Classify the preparation.
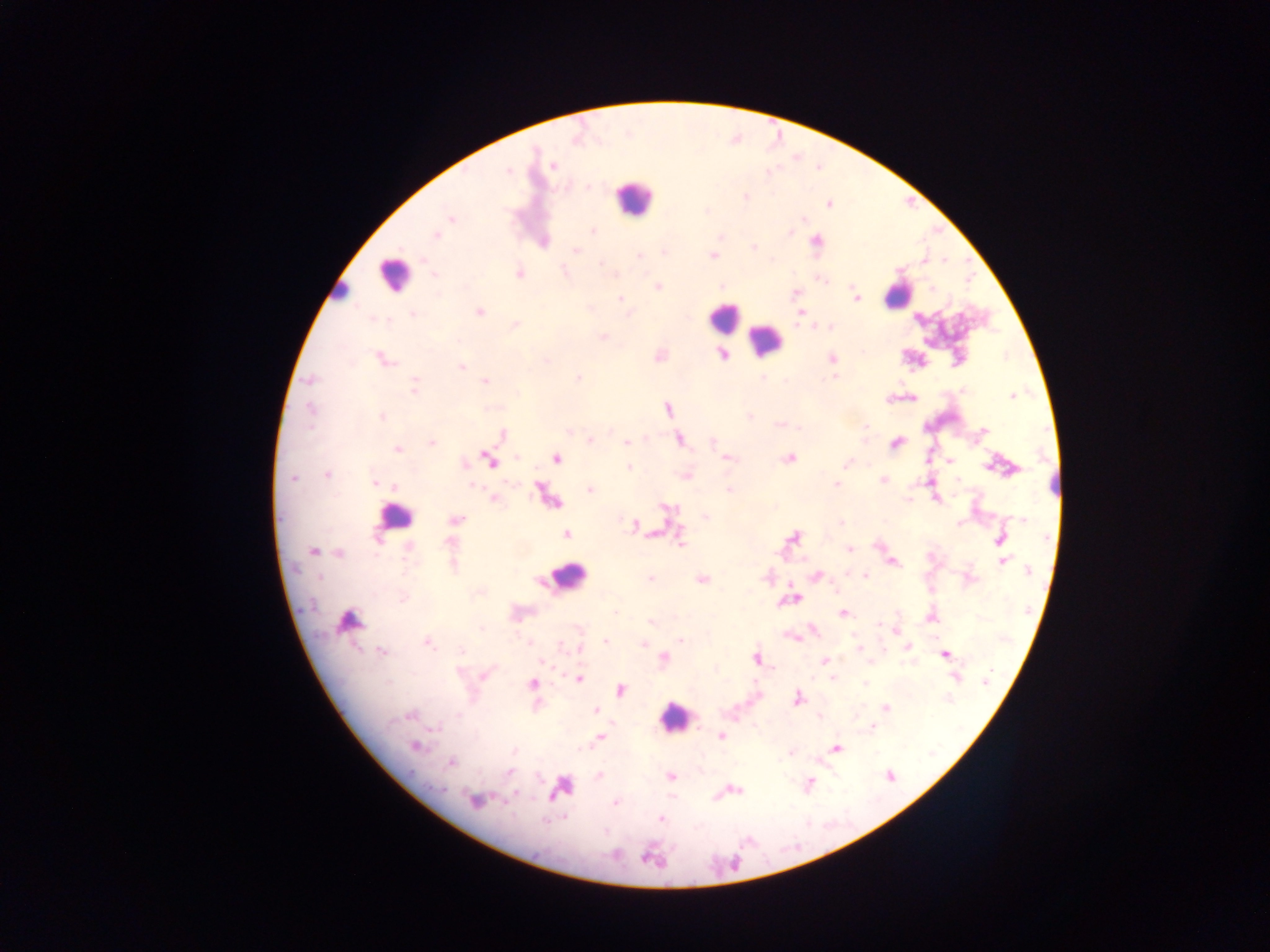
This is a thick smear.

Approximate centers as {x, y} in pixels. Plasmodium parasite locations: {553, 166}, {508, 171}, {746, 197}, {828, 204}, {451, 219}, {592, 231}, {791, 233}, {435, 236}, {816, 240}, {754, 246}, {576, 251}, {664, 252}, {638, 255}, {712, 255}, {601, 263}, {519, 273}, {433, 274}, {821, 280}, {723, 286}, {657, 287}, {796, 292}, {621, 298}, {856, 298}, {480, 311}, {799, 313}, {413, 315}, {374, 318}, {515, 324}, {814, 326}, {830, 327}, {603, 336}, {722, 354}, {831, 359}, {385, 360}, {545, 361}, {461, 366}, {834, 377}, {311, 379}, {578, 379}, {485, 381}, {415, 387}, {963, 391}, {1012, 397}, {668, 408}, {311, 409}, {381, 416}, {749, 416}, {778, 426}, {866, 426}, {798, 429}, {983, 430}, {502, 434}, {680, 439}, {590, 441}, {627, 442}, {712, 442}, {432, 443}, {895, 444}, {398, 449}, {516, 457}, {556, 458}, {728, 458}, {790, 459}, {489, 460}, {951, 461}, {845, 463}, {465, 464}, {988, 466}, {629, 467}, {327, 475}, {686, 476}, {293, 477}, {883, 479}, {375, 483}, {836, 484}, {394, 485}, {472, 486}, {590, 490}, {729, 490}, {494, 498}, {908, 500}, {705, 516}, {455, 519}, {1022, 519}, {840, 523}, {960, 524}, {633, 525}, {566, 535}, {793, 537}, {377, 539}, {680, 540}, {999, 540}, {450, 541}, {409, 547}, {849, 549}, {312, 551}, {339, 554}, {1003, 562}, {893, 563}, {454, 567}, {1030, 570}, {816, 576}, {866, 576}, {319, 578}, {650, 578}, {701, 579}, {403, 598}, {843, 612}, {615, 613}, {651, 622}, {879, 624}, {481, 628}, {813, 629}, {791, 636}, {681, 640}, {605, 641}, {427, 643}, {529, 643}, {644, 643}, {561, 645}, {908, 647}, {859, 648}, {580, 649}, {461, 651}, {382, 652}, {946, 655}, {756, 658}, {664, 659}, {825, 661}, {542, 663}, {485, 675}, {832, 678}, {955, 678}, {578, 679}, {388, 682}, {986, 682}, {532, 684}, {865, 684}, {621, 690}, {797, 698}, {886, 707}, {595, 711}, {409, 715}, {458, 715}, {819, 717}, {873, 727}, {437, 730}, {720, 736}, {600, 737}, {415, 746}, {837, 747}, {514, 751}, {790, 752}, {451, 762}, {510, 773}, {599, 776}, {891, 776}, {671, 777}, {810, 783}, {438, 788}, {559, 788}, {736, 790}, {514, 792}, {474, 801}, {615, 802}, {661, 818}, {546, 821}. Leukocyte locations: {633, 198}, {393, 275}, {341, 293}, {898, 297}, {723, 316}, {765, 340}, {394, 517}, {567, 576}, {348, 619}, {674, 716}. Photographed through a microscope with a mobile-phone camera. Sample from Ghana. Image is 1270×952 pixels. One field of view.